Describe the morphology of the red blood cells.
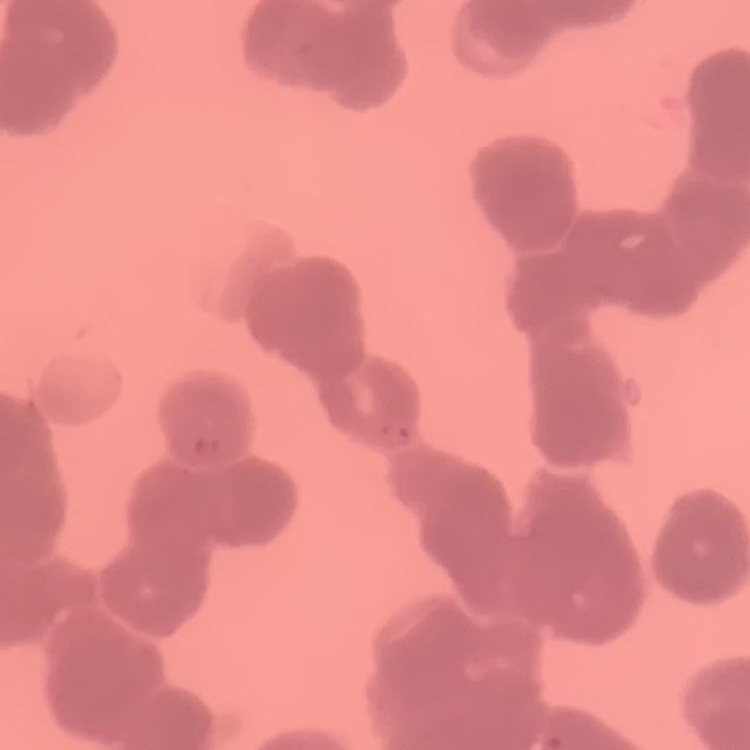

Rouleaux formation.

Stained with either Field's or Giemsa. One tile cut from a larger photomicrograph. Thin blood film.